State which parasite is depicted.
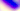
This is Toxoplasma gondii.

magnification = 400x
modality = photomicrograph